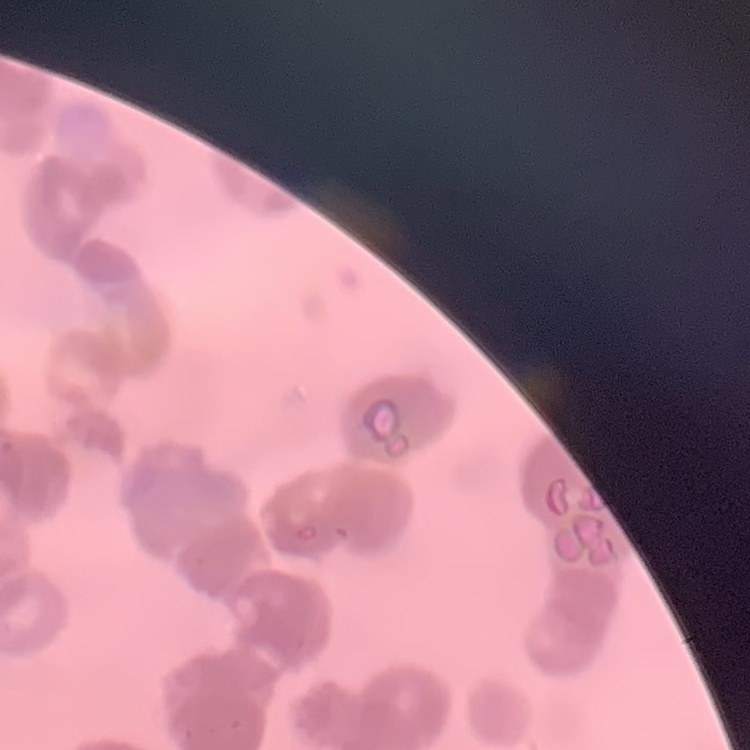
The red blood cells show rouleaux formation. Field's or Giemsa stain. Thin peripheral smear. Square crop of a larger photomicrograph.